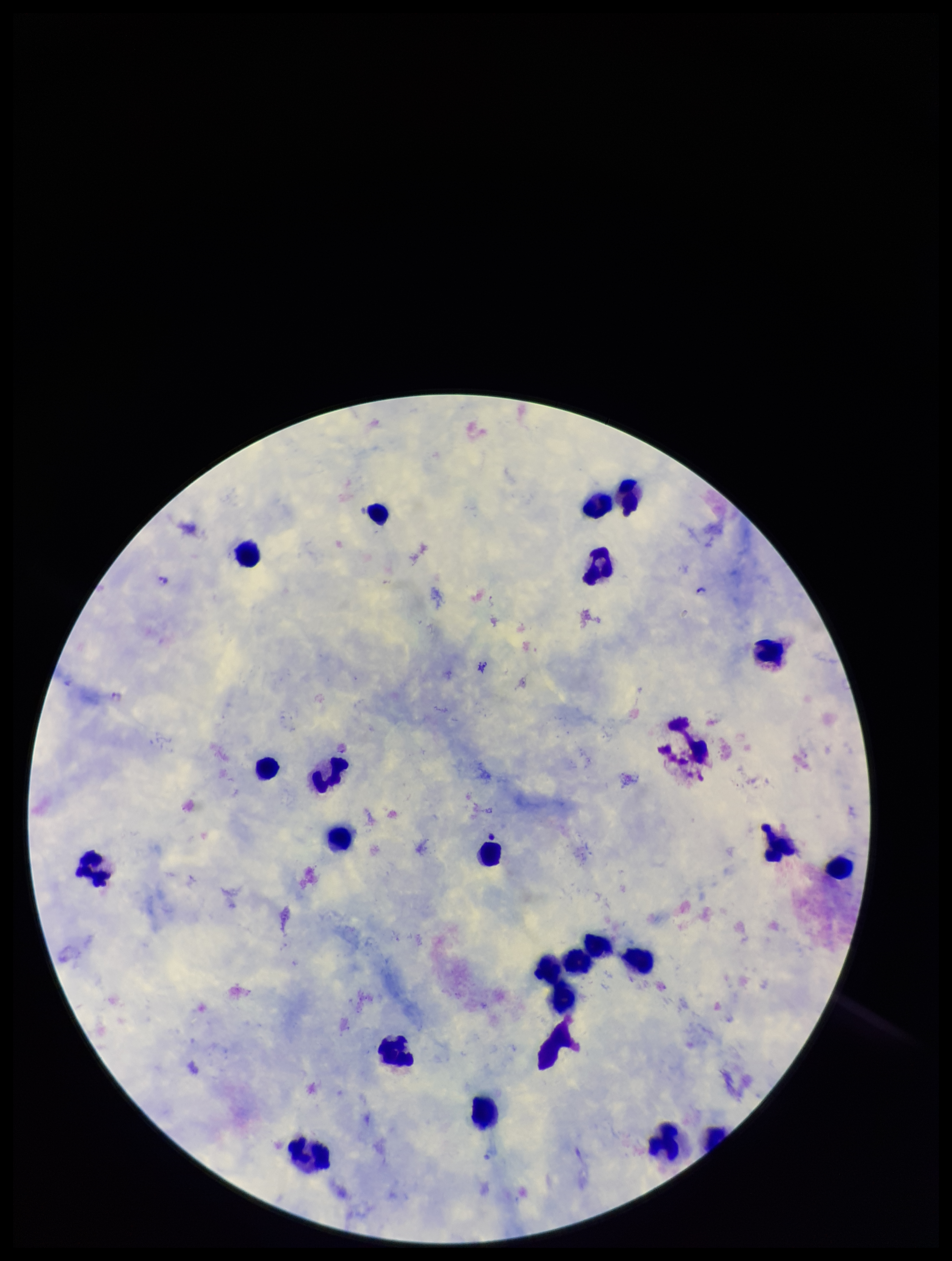
Species reported for this patient: Plasmodium falciparum. One field from this slide. Plasmodium parasites: seen. Parasite count: 1. Giemsa stain. Image is 952×1261 pixels. Leukocyte count: 23. Patient malaria status: positive. Preparation: thick smear. Photographed through the microscope eyepiece with a smartphone camera.